Name the parasite shown.
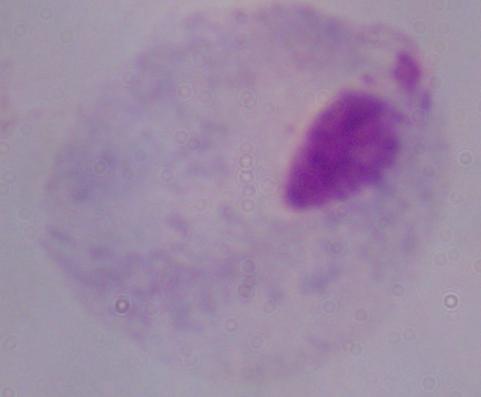

A trichomonad.

Photomicrograph. 1000x magnification.